Give the extent of all Plasmodium vivax-infected red blood cells.
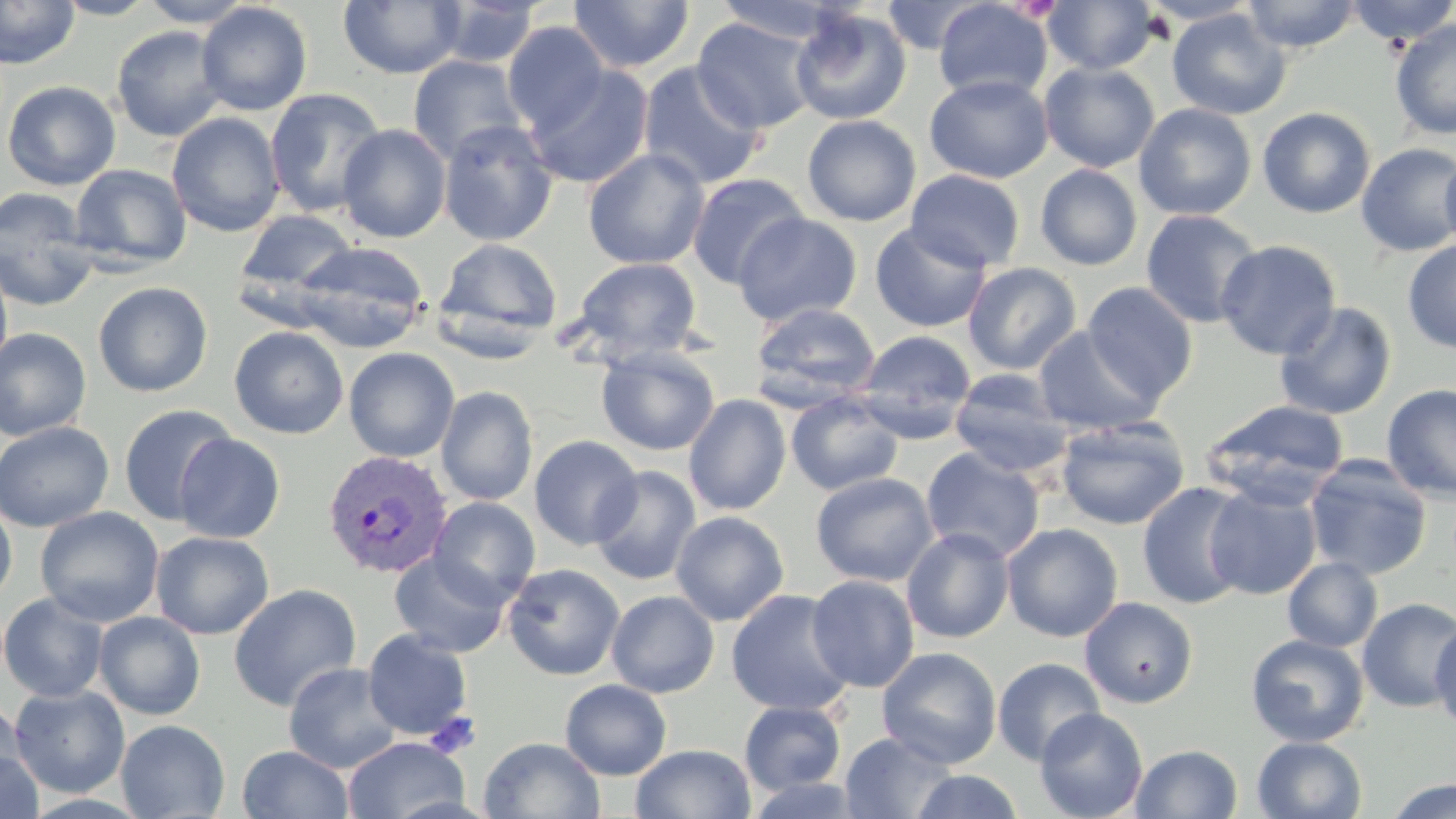
Approximate bounding boxes as (x1,y1)-(x2,y2) corner pairs in pixels.
Plasmodium vivax-infected red blood cells: (322,450)-(454,580).

Summary:
  - Platelet locations: (426,712)-(482,759)
  - Uninfected red blood cell locations: (0,0)-(80,69), (50,0)-(161,19), (137,0)-(258,28), (567,0)-(695,74), (1042,0)-(1158,74), (1242,0)-(1362,54), (1344,0)-(1456,46), (339,1)-(465,78), (432,1)-(542,68), (711,1)-(846,45), (933,1)-(1052,103), (195,2)-(313,116), (881,2)-(988,54), (790,7)-(911,126), (1167,9)-(1291,120), (692,16)-(819,134), (1390,19)-(1455,141), (502,21)-(610,135), (111,25)-(228,142), (407,55)-(529,166), (637,61)-(768,190), (1039,62)-(1160,173), (524,64)-(654,189), (924,74)-(1054,184), (2,80)-(121,191), (265,88)-(387,217), (1134,103)-(1257,220), (1258,106)-(1376,219), (167,112)-(285,237), (802,114)-(921,226), (437,120)-(558,246), (337,124)-(451,243), (1356,142)-(1456,258), (583,148)-(709,270), (1440,148)-(1456,256), (69,164)-(191,272), (1035,164)-(1143,271), (905,169)-(1025,273), (686,173)-(810,289), (0,186)-(100,311), (235,209)-(359,307), (1140,209)-(1264,329), (733,212)-(863,327), (869,222)-(992,333), (432,238)-(563,355), (1215,239)-(1341,360), (1402,239)-(1456,354), (293,242)-(430,353), (0,257)-(13,376), (571,257)-(702,363), (963,262)-(1081,375), (93,281)-(213,397), (1082,282)-(1199,404), (749,300)-(881,409), (1273,301)-(1397,421), (229,326)-(349,439), (1033,326)-(1162,435), (0,328)-(92,441), (855,330)-(977,441), (596,345)-(720,456), (344,347)-(460,463), (948,369)-(1074,477), (1382,384)-(1456,502), (436,386)-(538,506), (786,392)-(904,496), (683,394)-(791,516), (1201,399)-(1351,505), (118,404)-(239,526), (1055,416)-(1190,531), (0,421)-(114,533), (174,434)-(285,543), (529,435)-(643,551), (921,446)-(1045,562), (1304,455)-(1432,580), (589,465)-(701,586), (811,472)-(939,587), (1136,481)-(1254,610), (1204,483)-(1321,600), (428,496)-(541,608), (0,497)-(17,606), (35,506)-(164,627), (670,510)-(790,626), (1001,523)-(1123,642), (901,527)-(1015,644), (150,531)-(274,640), (389,552)-(511,658), (1283,557)-(1383,652), (502,562)-(625,681), (806,574)-(920,692), (228,584)-(362,712), (726,589)-(855,716), (606,590)-(720,698), (0,592)-(109,703), (1080,597)-(1198,708), (1357,597)-(1456,713), (94,611)-(206,720), (113,611)-(222,819), (1429,620)-(1456,729), (362,629)-(473,740), (1246,634)-(1369,746), (877,647)-(1002,768), (992,657)-(1106,766), (283,661)-(404,773), (560,679)-(672,780), (9,685)-(130,798), (1,696)-(29,798), (739,701)-(847,795), (1034,707)-(1148,819), (116,719)-(230,818), (840,731)-(958,819), (343,736)-(469,819), (478,736)-(606,819), (1252,736)-(1367,819), (631,744)-(756,819), (1131,744)-(1243,819), (236,745)-(354,819), (0,746)-(43,819), (910,770)-(1024,818), (742,775)-(870,818), (1383,778)-(1456,819)
  - Slide-level diagnosis: Plasmodium vivax
  - Image size: 1456×819 pixels
  - Modality: light microscopy
  - Magnification: 1000x
  - Preparation: thin blood film
  - Field of view: single
  - Stain: May-Grünwald-Giemsa